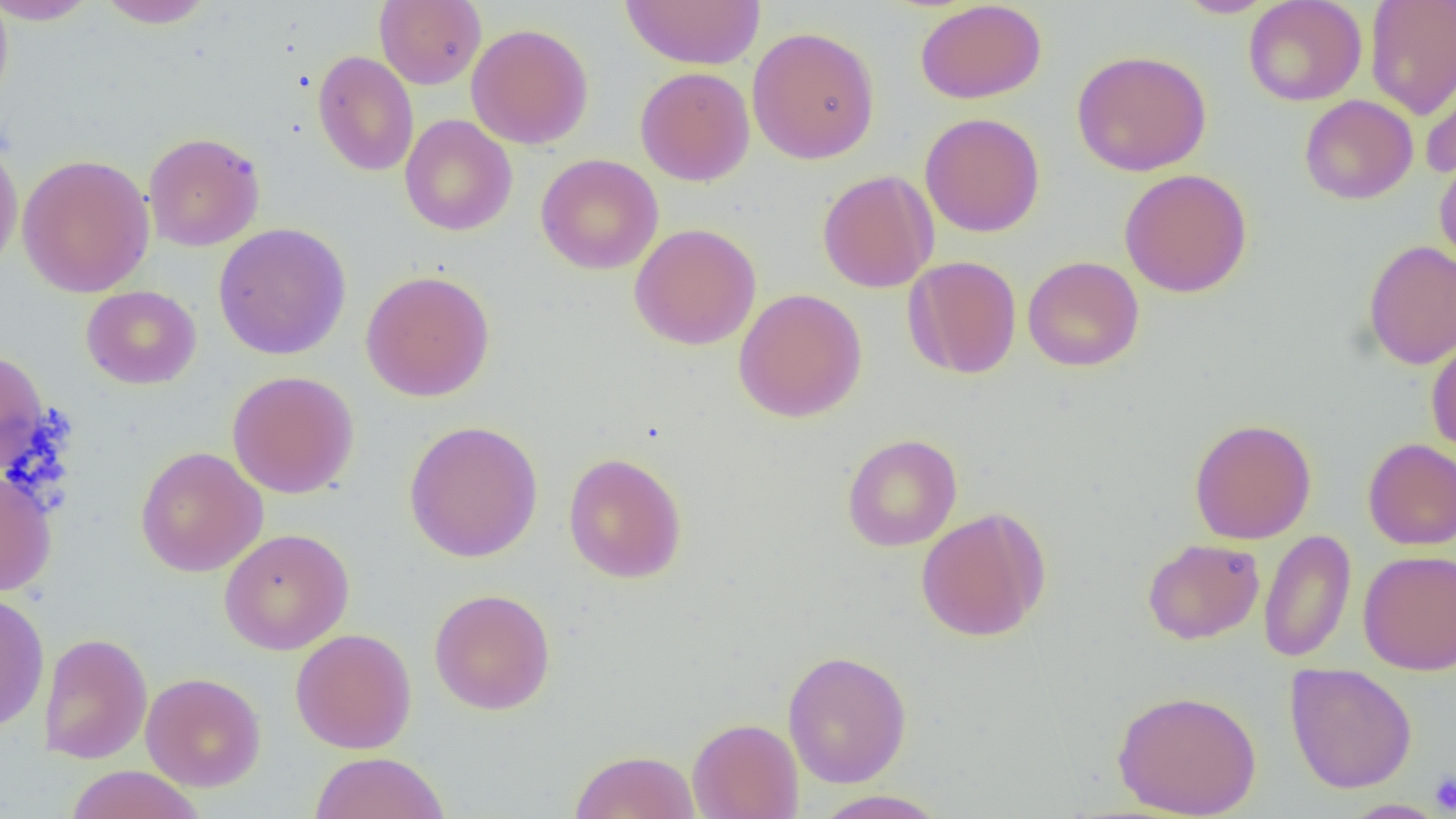

Approximate bounding boxes as [x1, y1, x2, y2] in pixels. Uninfected red blood cell locations: [0, 0, 13, 110], [95, 0, 217, 28], [1173, 0, 1278, 18], [1243, 0, 1367, 106], [1365, 0, 1456, 119], [0, 1, 99, 25], [374, 1, 487, 89], [621, 1, 766, 69], [914, 1, 1047, 104], [466, 23, 594, 149], [747, 26, 880, 165], [312, 50, 419, 176], [1072, 50, 1212, 176], [1419, 57, 1456, 179], [634, 67, 755, 186], [1299, 94, 1418, 205], [920, 112, 1045, 237], [399, 114, 517, 236], [142, 132, 265, 252], [0, 138, 23, 277], [1433, 152, 1456, 270], [16, 153, 156, 298], [535, 153, 664, 275], [1119, 168, 1253, 297], [817, 170, 939, 293], [213, 223, 352, 360], [629, 223, 761, 350], [1362, 239, 1456, 369], [904, 255, 1022, 380], [1022, 256, 1145, 372], [360, 269, 495, 402], [81, 285, 201, 389], [734, 288, 867, 422], [1426, 336, 1456, 456], [0, 349, 49, 473], [227, 370, 359, 498], [1189, 417, 1317, 544], [403, 420, 543, 563], [841, 433, 962, 552], [1362, 438, 1456, 550], [135, 446, 268, 577], [562, 451, 688, 584], [0, 469, 57, 597], [915, 508, 1050, 642], [219, 528, 354, 655], [1259, 529, 1356, 663], [1142, 538, 1265, 645], [1357, 549, 1456, 675], [429, 588, 556, 715], [0, 591, 50, 733], [290, 628, 417, 754], [38, 632, 153, 764], [782, 650, 912, 788], [1284, 663, 1418, 794], [141, 672, 266, 792], [1111, 689, 1263, 818], [687, 717, 804, 819], [569, 749, 701, 819], [310, 752, 450, 819], [64, 765, 206, 819], [811, 789, 948, 819], [1338, 799, 1449, 818]. Platelet locations: [1430, 770, 1456, 815]. Slide-level diagnosis: negative for blood parasites. 1000x magnification. Image is 1456×819 pixels. Light microscopy. Thin blood film. One field of a larger specimen.